Outline each Plasmodium falciparum-infected red blood cell.
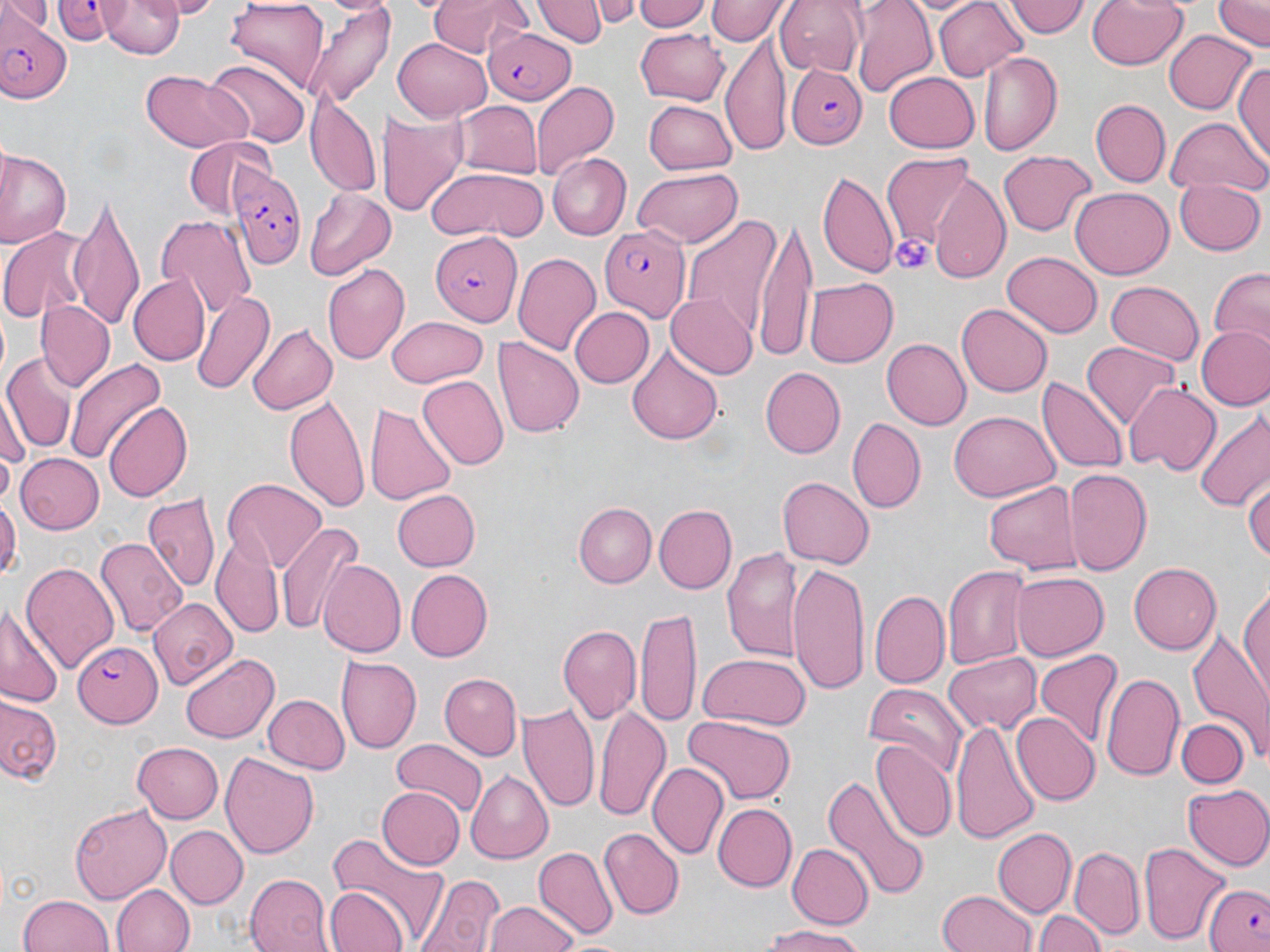
Approximate bounding boxes as named x1/y1/x2/y2 corners in pixels.
Plasmodium falciparum-infected red blood cells: (x1=52, y1=0, x2=136, y2=46), (x1=2, y1=14, x2=73, y2=105), (x1=484, y1=28, x2=577, y2=106), (x1=788, y1=64, x2=866, y2=148), (x1=231, y1=171, x2=300, y2=268), (x1=597, y1=222, x2=688, y2=320), (x1=431, y1=231, x2=522, y2=324), (x1=71, y1=643, x2=161, y2=724), (x1=1203, y1=878, x2=1269, y2=952).

{
  "slide_level_diagnosis": "Plasmodium falciparum",
  "modality": "optical microscopy",
  "preparation": "thin blood smear",
  "field_of_view": "single",
  "image_size": "1270×952 pixels",
  "platelet_locations": "approximate bounding boxes as named x1/y1/x2/y2 corners in pixels: (x1=889, y1=233, x2=935, y2=275)",
  "uninfected_red_blood_cell_locations": "approximate bounding boxes as named x1/y1/x2/y2 corners in pixels: (x1=3, y1=0, x2=52, y2=40), (x1=165, y1=0, x2=218, y2=17), (x1=424, y1=0, x2=531, y2=56), (x1=537, y1=0, x2=605, y2=48), (x1=634, y1=0, x2=714, y2=33), (x1=773, y1=0, x2=863, y2=73), (x1=850, y1=0, x2=937, y2=97), (x1=934, y1=0, x2=1027, y2=80), (x1=1003, y1=0, x2=1089, y2=40), (x1=1087, y1=0, x2=1187, y2=71), (x1=1213, y1=0, x2=1268, y2=51), (x1=101, y1=1, x2=189, y2=59), (x1=226, y1=1, x2=331, y2=90), (x1=591, y1=1, x2=643, y2=27), (x1=705, y1=1, x2=788, y2=46), (x1=299, y1=5, x2=395, y2=109), (x1=636, y1=29, x2=730, y2=105), (x1=1164, y1=29, x2=1259, y2=115), (x1=720, y1=34, x2=791, y2=153), (x1=392, y1=39, x2=490, y2=121), (x1=978, y1=49, x2=1064, y2=158), (x1=204, y1=57, x2=312, y2=145), (x1=1232, y1=61, x2=1270, y2=160), (x1=140, y1=70, x2=255, y2=152), (x1=883, y1=70, x2=980, y2=153), (x1=533, y1=84, x2=619, y2=175), (x1=306, y1=94, x2=381, y2=195), (x1=454, y1=99, x2=544, y2=180), (x1=644, y1=99, x2=737, y2=174), (x1=1091, y1=99, x2=1170, y2=187), (x1=379, y1=112, x2=468, y2=217), (x1=1165, y1=116, x2=1267, y2=198), (x1=183, y1=137, x2=273, y2=218), (x1=1, y1=149, x2=71, y2=245), (x1=999, y1=150, x2=1096, y2=238), (x1=548, y1=153, x2=630, y2=241), (x1=882, y1=153, x2=979, y2=251), (x1=425, y1=167, x2=549, y2=241), (x1=632, y1=168, x2=743, y2=247), (x1=818, y1=171, x2=898, y2=277), (x1=929, y1=173, x2=1009, y2=283), (x1=1172, y1=177, x2=1265, y2=255), (x1=1069, y1=188, x2=1172, y2=279), (x1=303, y1=189, x2=396, y2=280), (x1=68, y1=196, x2=147, y2=330), (x1=680, y1=213, x2=779, y2=343), (x1=154, y1=214, x2=256, y2=317), (x1=753, y1=214, x2=818, y2=364), (x1=0, y1=228, x2=90, y2=323), (x1=513, y1=251, x2=602, y2=355), (x1=1003, y1=251, x2=1102, y2=339), (x1=324, y1=262, x2=410, y2=364), (x1=1206, y1=268, x2=1270, y2=352), (x1=128, y1=275, x2=209, y2=364), (x1=805, y1=277, x2=898, y2=366), (x1=1105, y1=280, x2=1202, y2=366), (x1=192, y1=289, x2=275, y2=398), (x1=666, y1=292, x2=757, y2=379), (x1=35, y1=300, x2=114, y2=392), (x1=957, y1=305, x2=1053, y2=397), (x1=568, y1=306, x2=654, y2=389), (x1=388, y1=316, x2=489, y2=387), (x1=246, y1=323, x2=336, y2=415), (x1=1196, y1=325, x2=1269, y2=408), (x1=494, y1=337, x2=585, y2=438), (x1=883, y1=339, x2=971, y2=428), (x1=1083, y1=342, x2=1181, y2=429), (x1=625, y1=345, x2=724, y2=445), (x1=3, y1=356, x2=76, y2=455), (x1=68, y1=356, x2=166, y2=462), (x1=759, y1=367, x2=844, y2=457), (x1=419, y1=376, x2=508, y2=470), (x1=1040, y1=377, x2=1127, y2=475), (x1=1126, y1=384, x2=1219, y2=474), (x1=284, y1=392, x2=372, y2=517), (x1=364, y1=400, x2=458, y2=508), (x1=104, y1=401, x2=194, y2=502), (x1=1191, y1=406, x2=1270, y2=511), (x1=949, y1=411, x2=1058, y2=504), (x1=847, y1=417, x2=925, y2=514), (x1=16, y1=453, x2=105, y2=534), (x1=1064, y1=469, x2=1151, y2=575), (x1=1244, y1=474, x2=1270, y2=567), (x1=778, y1=477, x2=874, y2=568), (x1=223, y1=478, x2=325, y2=570), (x1=982, y1=480, x2=1084, y2=574), (x1=391, y1=487, x2=480, y2=571), (x1=143, y1=490, x2=220, y2=594), (x1=0, y1=493, x2=18, y2=583), (x1=652, y1=502, x2=736, y2=595), (x1=574, y1=503, x2=655, y2=588), (x1=277, y1=526, x2=359, y2=635), (x1=94, y1=536, x2=185, y2=636), (x1=212, y1=537, x2=284, y2=635), (x1=720, y1=545, x2=804, y2=665), (x1=318, y1=559, x2=404, y2=658), (x1=21, y1=561, x2=119, y2=676), (x1=1129, y1=561, x2=1224, y2=654), (x1=944, y1=563, x2=1031, y2=667), (x1=787, y1=564, x2=871, y2=693), (x1=406, y1=569, x2=493, y2=661), (x1=1009, y1=572, x2=1107, y2=661), (x1=1239, y1=585, x2=1269, y2=705), (x1=870, y1=589, x2=950, y2=686), (x1=148, y1=598, x2=238, y2=690), (x1=0, y1=603, x2=65, y2=711), (x1=638, y1=609, x2=703, y2=728), (x1=557, y1=624, x2=642, y2=726), (x1=1189, y1=626, x2=1270, y2=754), (x1=696, y1=652, x2=807, y2=729), (x1=1034, y1=652, x2=1121, y2=746), (x1=181, y1=653, x2=279, y2=744), (x1=943, y1=653, x2=1040, y2=734), (x1=335, y1=655, x2=422, y2=753), (x1=439, y1=672, x2=522, y2=757), (x1=1101, y1=672, x2=1186, y2=782), (x1=864, y1=682, x2=968, y2=779), (x1=264, y1=694, x2=351, y2=776), (x1=0, y1=695, x2=63, y2=787), (x1=517, y1=698, x2=598, y2=813), (x1=594, y1=700, x2=670, y2=820), (x1=1011, y1=713, x2=1099, y2=805), (x1=680, y1=714, x2=797, y2=805), (x1=950, y1=717, x2=1040, y2=846), (x1=1176, y1=718, x2=1249, y2=787), (x1=391, y1=740, x2=488, y2=817), (x1=870, y1=741, x2=956, y2=844), (x1=134, y1=742, x2=224, y2=822), (x1=220, y1=750, x2=319, y2=859), (x1=648, y1=762, x2=728, y2=860), (x1=465, y1=771, x2=553, y2=863), (x1=820, y1=775, x2=930, y2=900), (x1=1185, y1=784, x2=1270, y2=870), (x1=376, y1=786, x2=465, y2=871), (x1=70, y1=802, x2=172, y2=904), (x1=712, y1=803, x2=796, y2=893), (x1=166, y1=826, x2=247, y2=907), (x1=600, y1=828, x2=684, y2=918), (x1=994, y1=828, x2=1077, y2=915), (x1=322, y1=838, x2=447, y2=952), (x1=787, y1=844, x2=873, y2=929), (x1=1140, y1=844, x2=1230, y2=943), (x1=534, y1=845, x2=618, y2=938), (x1=1072, y1=846, x2=1145, y2=937), (x1=245, y1=873, x2=333, y2=952), (x1=413, y1=873, x2=509, y2=952), (x1=111, y1=884, x2=193, y2=952), (x1=325, y1=885, x2=409, y2=952), (x1=939, y1=890, x2=1038, y2=952), (x1=20, y1=894, x2=115, y2=952), (x1=485, y1=900, x2=575, y2=952), (x1=1035, y1=908, x2=1109, y2=952), (x1=763, y1=926, x2=871, y2=951)",
  "stain": "May-Grünwald-Giemsa",
  "magnification": "1000x"
}